Name the cell type shown.
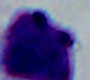
A leukocyte.

1000x magnification. Photomicrograph.